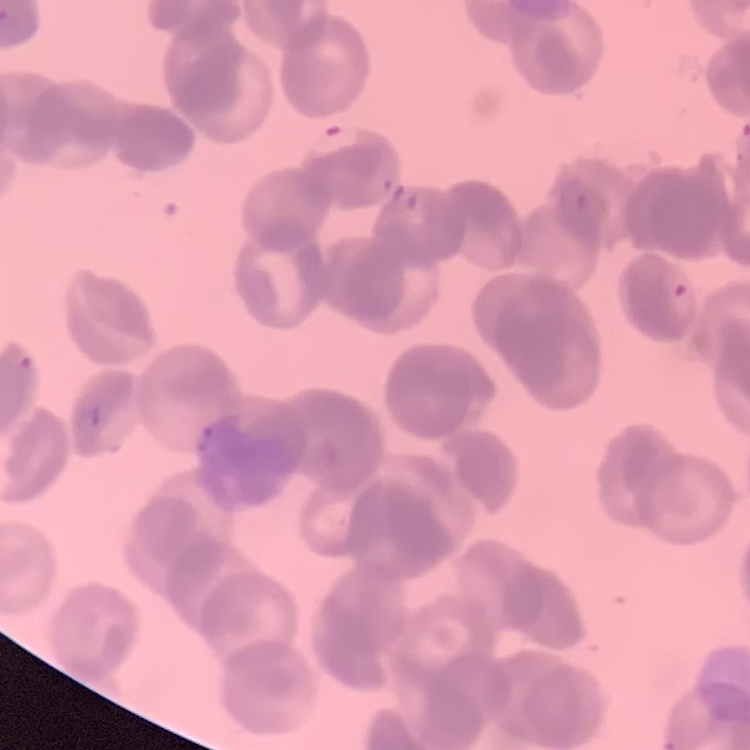

red_blood_cell_morphology: rouleaux formation
stain: Field's or Giemsa
preparation: thin blood smear
image_type: one tile cut from a larger photomicrograph